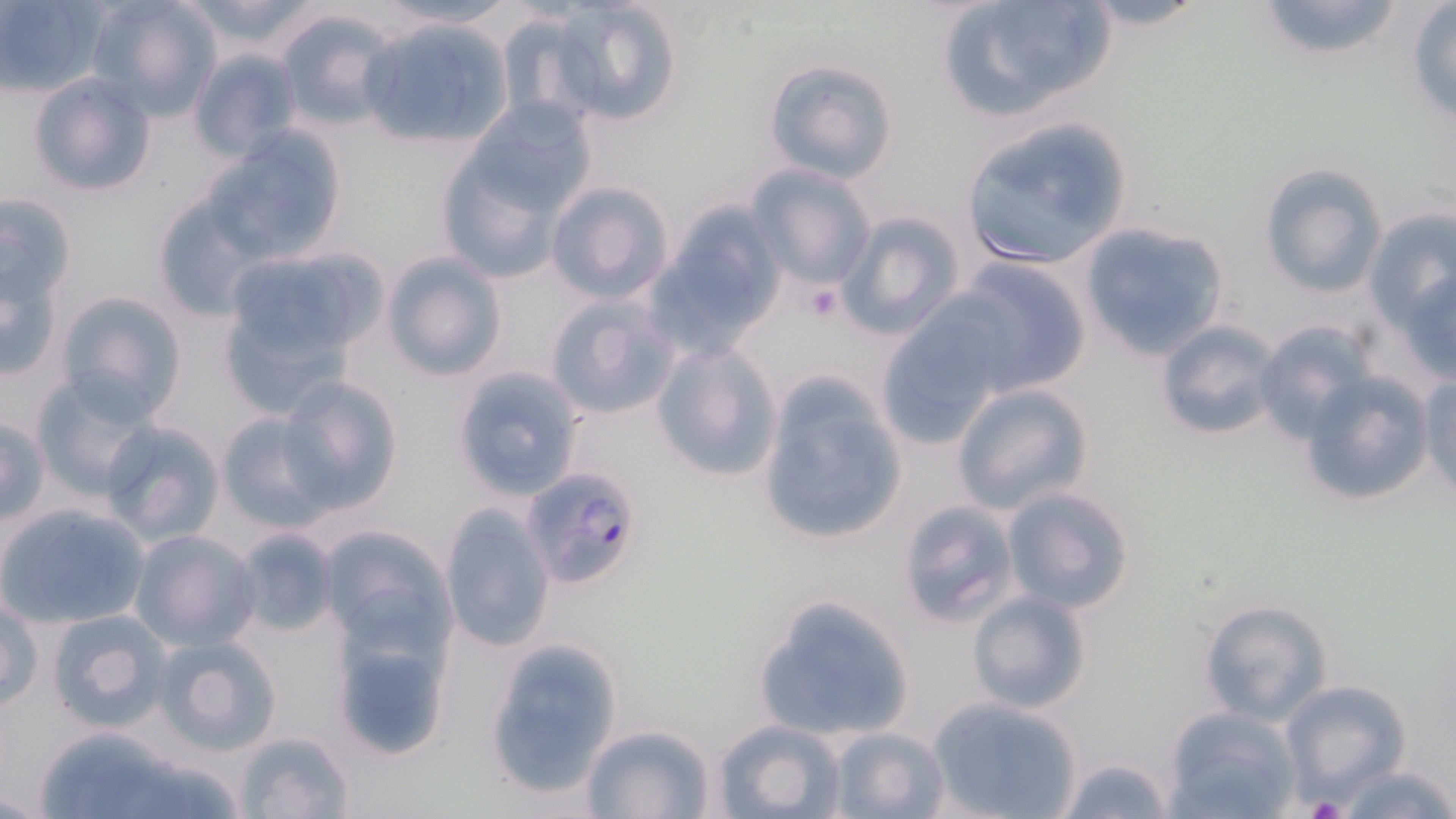 Approximate bounding boxes as named x1/y1/x2/y2 corners in pixels. Plasmodium falciparum-infected red blood cell locations: (x1=520, y1=464, x2=646, y2=588). Uninfected red blood cell locations: (x1=87, y1=0, x2=220, y2=119), (x1=172, y1=0, x2=332, y2=57), (x1=372, y1=0, x2=517, y2=31), (x1=547, y1=0, x2=685, y2=127), (x1=934, y1=0, x2=1118, y2=123), (x1=1074, y1=0, x2=1216, y2=32), (x1=1251, y1=0, x2=1410, y2=65), (x1=1, y1=1, x2=105, y2=96), (x1=1406, y1=4, x2=1456, y2=125), (x1=275, y1=9, x2=400, y2=131), (x1=492, y1=9, x2=605, y2=125), (x1=356, y1=15, x2=512, y2=149), (x1=186, y1=48, x2=301, y2=162), (x1=762, y1=57, x2=898, y2=183), (x1=28, y1=73, x2=158, y2=199), (x1=464, y1=98, x2=598, y2=218), (x1=957, y1=116, x2=1138, y2=270), (x1=207, y1=128, x2=349, y2=261), (x1=432, y1=152, x2=567, y2=284), (x1=746, y1=163, x2=877, y2=290), (x1=1258, y1=163, x2=1386, y2=297), (x1=544, y1=181, x2=673, y2=303), (x1=0, y1=190, x2=78, y2=312), (x1=148, y1=190, x2=268, y2=323), (x1=653, y1=200, x2=789, y2=353), (x1=1360, y1=205, x2=1454, y2=336), (x1=832, y1=209, x2=965, y2=339), (x1=1078, y1=221, x2=1231, y2=360), (x1=217, y1=248, x2=381, y2=379), (x1=2, y1=249, x2=65, y2=384), (x1=381, y1=251, x2=507, y2=382), (x1=1388, y1=256, x2=1456, y2=386), (x1=946, y1=257, x2=1094, y2=398), (x1=56, y1=290, x2=187, y2=418), (x1=542, y1=293, x2=682, y2=421), (x1=875, y1=309, x2=1009, y2=448), (x1=1154, y1=319, x2=1284, y2=442), (x1=1253, y1=320, x2=1378, y2=443), (x1=651, y1=340, x2=784, y2=482), (x1=450, y1=366, x2=586, y2=502), (x1=1294, y1=368, x2=1436, y2=511), (x1=755, y1=369, x2=911, y2=548), (x1=1417, y1=369, x2=1456, y2=500), (x1=29, y1=373, x2=159, y2=501), (x1=276, y1=379, x2=405, y2=516), (x1=951, y1=381, x2=1096, y2=515), (x1=215, y1=410, x2=331, y2=531), (x1=0, y1=417, x2=50, y2=526), (x1=98, y1=420, x2=226, y2=546), (x1=999, y1=484, x2=1139, y2=613), (x1=895, y1=497, x2=1022, y2=627), (x1=1, y1=501, x2=152, y2=629), (x1=440, y1=505, x2=556, y2=652), (x1=319, y1=523, x2=456, y2=653), (x1=229, y1=527, x2=338, y2=638), (x1=129, y1=529, x2=260, y2=649), (x1=966, y1=590, x2=1093, y2=715), (x1=749, y1=593, x2=918, y2=742), (x1=2, y1=594, x2=42, y2=713), (x1=1196, y1=598, x2=1333, y2=725), (x1=44, y1=608, x2=174, y2=733), (x1=330, y1=626, x2=455, y2=763), (x1=152, y1=634, x2=284, y2=757), (x1=482, y1=639, x2=623, y2=799), (x1=1280, y1=679, x2=1414, y2=802), (x1=924, y1=696, x2=1082, y2=819), (x1=1162, y1=706, x2=1301, y2=819), (x1=713, y1=716, x2=848, y2=819), (x1=577, y1=722, x2=718, y2=819), (x1=29, y1=726, x2=232, y2=819), (x1=824, y1=726, x2=949, y2=819), (x1=230, y1=729, x2=359, y2=819), (x1=1052, y1=753, x2=1176, y2=819), (x1=1331, y1=762, x2=1455, y2=819). Platelet locations: (x1=803, y1=281, x2=843, y2=322), (x1=1302, y1=795, x2=1352, y2=819). Slide-level diagnosis: Plasmodium falciparum. May-Grünwald-Giemsa stain. Thin blood smear. Optical microscopy. Captured at 1000x magnification. Single field of view. Image is 1456×819 pixels.